Assess this cell for malaria.
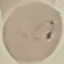
Parasitized.

Summary:
  - Preparation: thin smear
  - Capture: smartphone through the microscope eyepiece
  - Image type: automatically extracted cell patch, resized to 64 × 64 pixels
  - Stain: Giemsa